Report the malaria status of this cell.
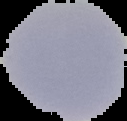
Uninfected.

Image is 127×121 pixels. From a thin blood film. Segmented cell region on a black background.